Name the parasite shown.
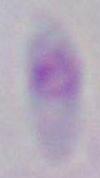
This is Toxoplasma gondii.

1000x magnification. Photomicrograph.